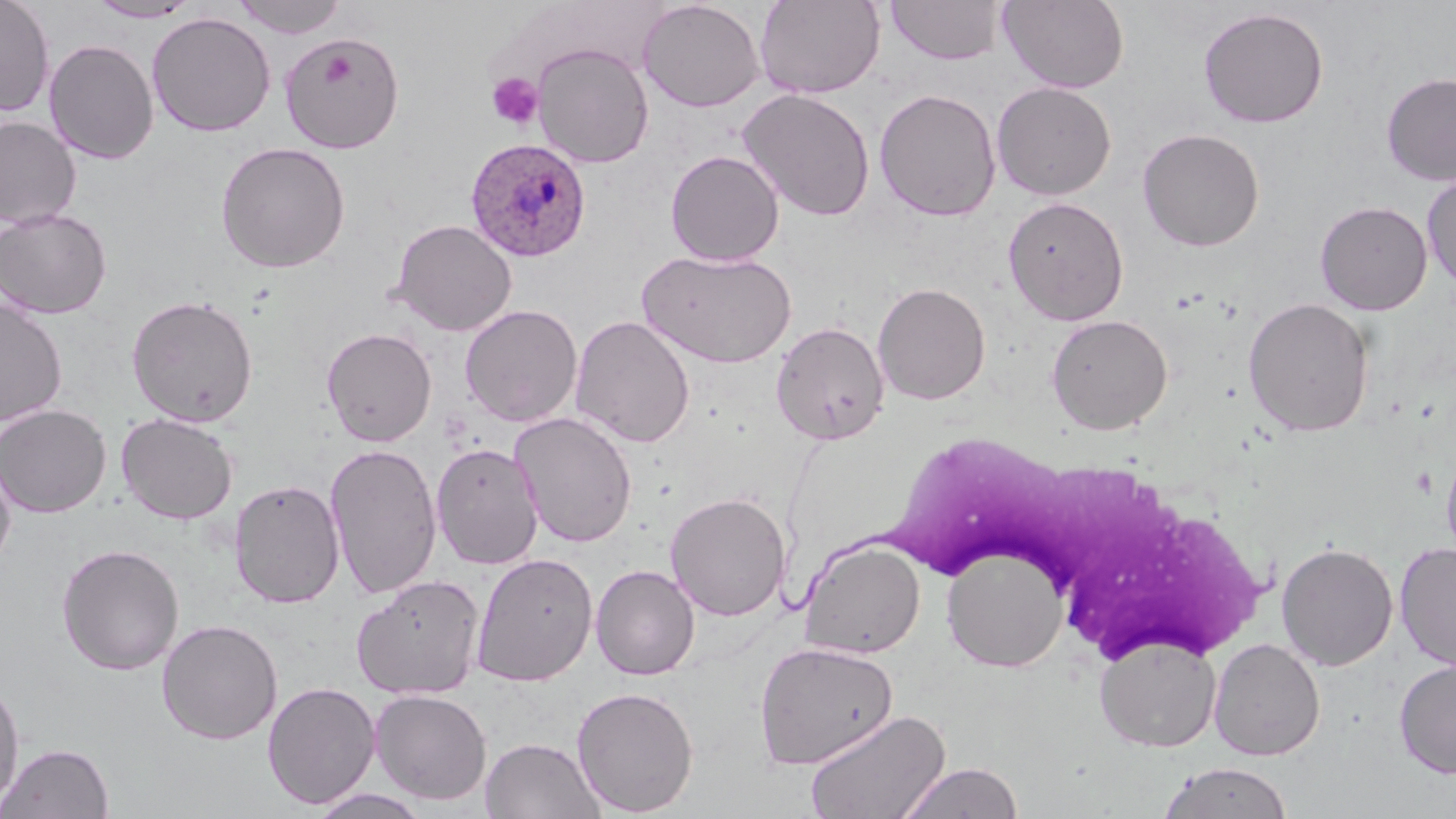
slide-level diagnosis = Plasmodium ovale
platelet locations = approximate bounding boxes as (x1,y1)-(x2,y2) corner pairs in pixels: (487,72)-(543,130)
preparation = thin blood smear
magnification = 1000x
modality = light microscopy
stain = May-Grünwald-Giemsa
image size = 1456×819 pixels
field of view = single
white blood cell locations = approximate bounding boxes as (x1,y1)-(x2,y2) corner pairs in pixels: (890,442)-(1270,656)
Plasmodium ovale-infected red blood cell locations = approximate bounding boxes as (x1,y1)-(x2,y2) corner pairs in pixels: (464,137)-(591,262)
uninfected red blood cell locations = approximate bounding boxes as (x1,y1)-(x2,y2) corner pairs in pixels: (0,0)-(55,117), (231,0)-(348,39), (755,0)-(885,99), (998,0)-(1129,92), (88,1)-(201,22), (637,1)-(765,112), (885,1)-(1007,65), (1197,6)-(1330,128), (146,12)-(276,137), (280,33)-(405,153), (43,39)-(159,164), (532,42)-(654,168), (1380,72)-(1456,186), (991,81)-(1116,200), (737,88)-(876,221), (874,88)-(1001,221), (0,116)-(81,228), (1137,128)-(1265,252), (215,141)-(351,274), (665,150)-(784,266), (1422,173)-(1456,292), (1002,196)-(1129,325), (1315,200)-(1433,315), (0,207)-(112,319), (389,219)-(517,336), (637,247)-(797,368), (872,282)-(991,405), (126,294)-(259,427), (1242,297)-(1376,437), (0,298)-(68,426), (459,304)-(583,427), (1046,314)-(1173,434), (569,315)-(696,448), (770,321)-(890,445), (321,327)-(437,447), (0,404)-(112,518), (509,411)-(638,548), (115,413)-(239,525), (431,442)-(544,569), (325,443)-(442,600), (1440,444)-(1456,563), (0,454)-(16,576), (229,478)-(345,608), (665,492)-(791,621), (798,537)-(926,659), (1276,542)-(1398,671), (1394,542)-(1456,672), (56,543)-(185,676), (941,544)-(1068,671), (471,552)-(598,687), (590,564)-(700,680), (351,575)-(484,699), (156,618)-(282,745), (1094,634)-(1221,751), (1209,638)-(1326,760), (753,640)-(900,769), (1394,659)-(1456,779), (0,676)-(25,811), (262,681)-(381,809), (571,685)-(700,816), (368,688)-(493,805), (804,709)-(950,819), (480,737)-(606,819), (1,742)-(115,818), (896,761)-(1025,819), (1159,761)-(1294,819), (307,788)-(433,818)